Outline each uninfected red blood cell.
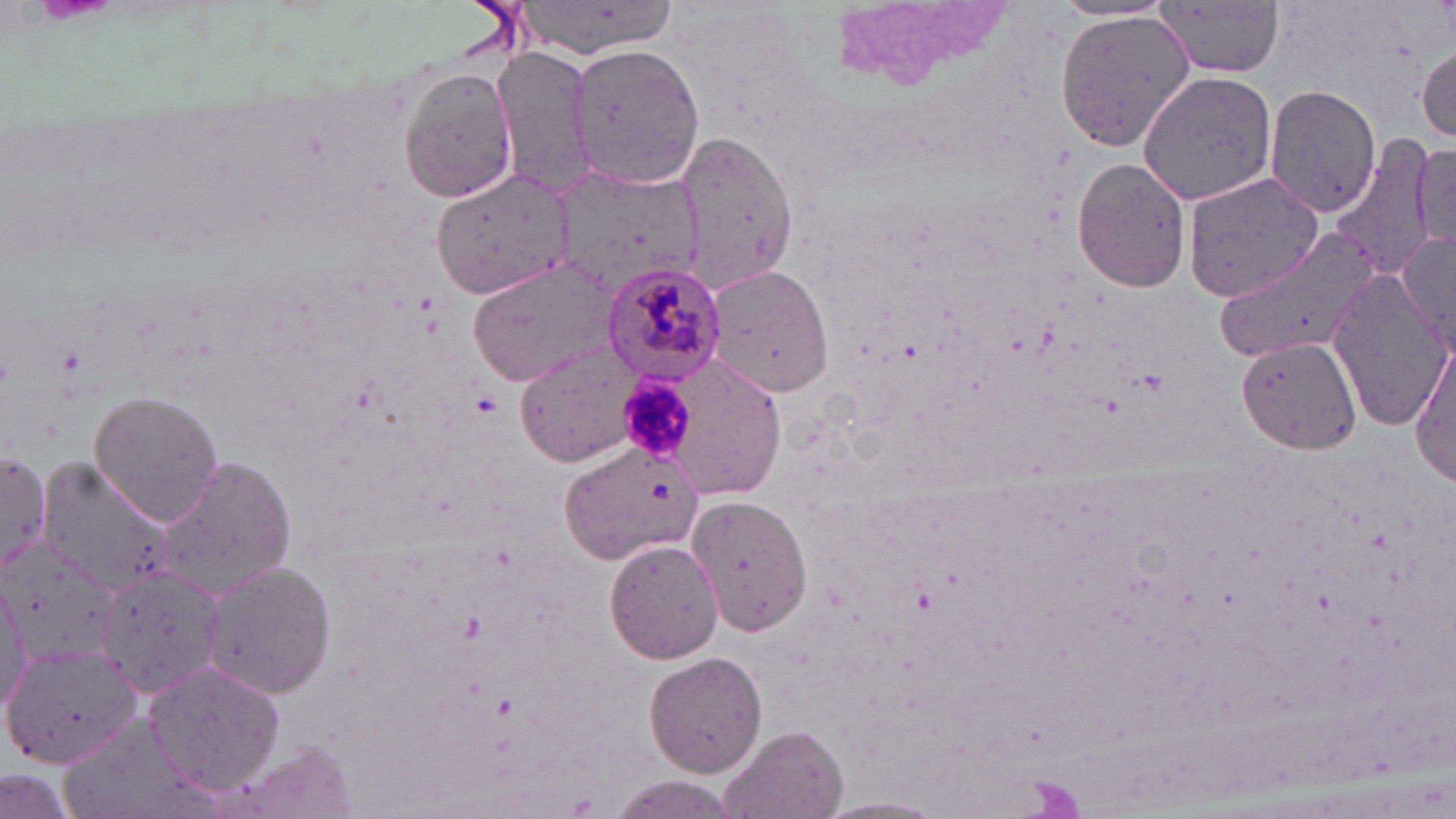

Approximate bounding boxes as named x1/y1/x2/y2 corners in pixels.
Uninfected red blood cells: (x1=503, y1=1, x2=684, y2=60), (x1=1155, y1=3, x2=1287, y2=76), (x1=1054, y1=13, x2=1196, y2=151), (x1=570, y1=40, x2=704, y2=190), (x1=1416, y1=45, x2=1454, y2=142), (x1=492, y1=46, x2=596, y2=195), (x1=394, y1=62, x2=520, y2=206), (x1=1138, y1=71, x2=1280, y2=206), (x1=1264, y1=82, x2=1383, y2=216), (x1=673, y1=129, x2=803, y2=294), (x1=1338, y1=133, x2=1439, y2=284), (x1=1409, y1=143, x2=1456, y2=252), (x1=1073, y1=158, x2=1194, y2=292), (x1=556, y1=165, x2=702, y2=295), (x1=429, y1=167, x2=576, y2=303), (x1=1182, y1=170, x2=1322, y2=304), (x1=1222, y1=227, x2=1382, y2=361), (x1=1396, y1=228, x2=1456, y2=350), (x1=467, y1=255, x2=623, y2=390), (x1=703, y1=264, x2=836, y2=398), (x1=1326, y1=273, x2=1456, y2=432), (x1=1235, y1=335, x2=1363, y2=454), (x1=517, y1=342, x2=644, y2=466), (x1=1410, y1=344, x2=1455, y2=487), (x1=681, y1=351, x2=789, y2=506), (x1=88, y1=391, x2=225, y2=525), (x1=559, y1=440, x2=708, y2=565), (x1=1, y1=446, x2=48, y2=583), (x1=154, y1=455, x2=298, y2=598), (x1=37, y1=460, x2=171, y2=596), (x1=687, y1=495, x2=812, y2=635), (x1=1, y1=535, x2=120, y2=666), (x1=605, y1=537, x2=725, y2=663), (x1=201, y1=560, x2=337, y2=699), (x1=100, y1=566, x2=223, y2=698), (x1=0, y1=585, x2=31, y2=714), (x1=1, y1=643, x2=142, y2=770), (x1=642, y1=650, x2=768, y2=777), (x1=146, y1=658, x2=285, y2=792), (x1=720, y1=725, x2=848, y2=819), (x1=228, y1=738, x2=362, y2=819), (x1=0, y1=767, x2=83, y2=819), (x1=605, y1=775, x2=743, y2=819), (x1=816, y1=796, x2=948, y2=818).

Summary:
  - Platelet locations: (x1=622, y1=379, x2=694, y2=458)
  - Plasmodium malariae-infected red blood cell locations: (x1=601, y1=259, x2=725, y2=387)
  - Slide-level diagnosis: Plasmodium malariae
  - Preparation: thin blood smear
  - Magnification: 1000x
  - Modality: optical microscopy
  - Stain: May-Grünwald-Giemsa
  - Image size: 1456×819 pixels
  - Field of view: one of a larger specimen